Locate every Plasmodium malariae-infected red blood cell.
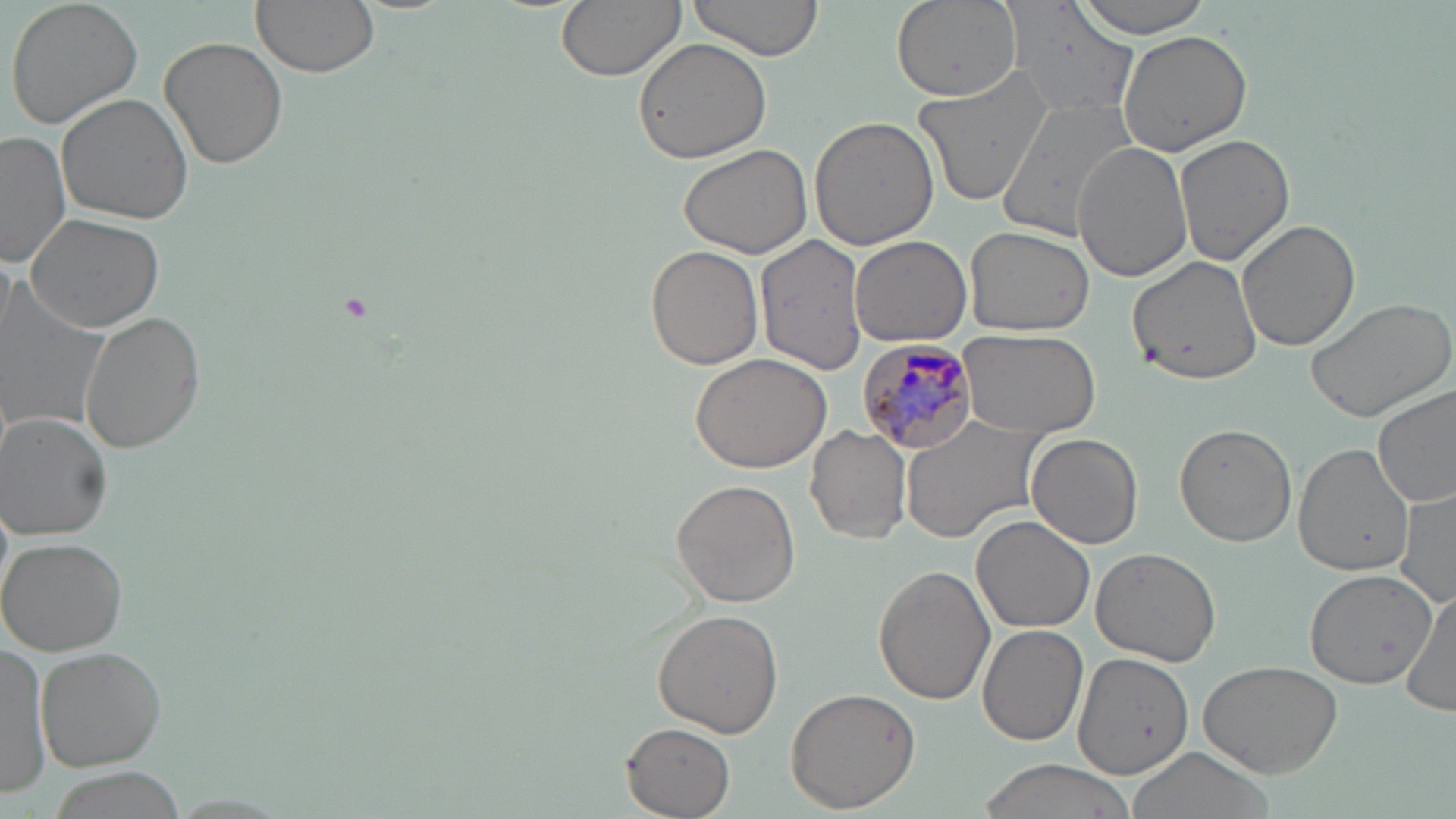
Approximate bounding boxes as (x1,y1)-(x2,y2) corner pairs in pixels.
Plasmodium malariae-infected red blood cells: (856,339)-(983,457).

slide-level diagnosis = Plasmodium malariae
preparation = thin blood smear
magnification = 1000x
stain = May-Grünwald-Giemsa
uninfected red blood cell locations = approximate bounding boxes as (x1,y1)-(x2,y2) corner pairs in pixels: (4,0)-(145,131), (251,0)-(378,77), (556,0)-(683,80), (684,0)-(827,65), (890,0)-(1022,102), (1069,0)-(1215,38), (1003,2)-(1138,117), (1118,29)-(1253,156), (159,36)-(290,170), (633,37)-(773,166), (914,69)-(1056,210), (57,93)-(193,225), (995,96)-(1140,242), (811,116)-(938,251), (0,131)-(72,268), (1174,134)-(1293,265), (676,141)-(812,258), (1073,142)-(1196,282), (27,212)-(167,332), (1236,219)-(1360,353), (964,223)-(1096,335), (755,236)-(870,376), (849,236)-(971,348), (644,246)-(762,370), (1126,252)-(1262,385), (1,276)-(111,434), (1304,295)-(1455,423), (78,310)-(206,454), (958,327)-(1099,438), (688,352)-(833,474), (1374,384)-(1456,509), (901,412)-(1047,543), (3,413)-(115,540), (1175,422)-(1297,546), (807,426)-(912,545), (1027,433)-(1144,549), (1293,441)-(1416,576), (671,479)-(802,608), (1398,488)-(1456,610), (972,515)-(1094,635), (2,537)-(127,656), (1092,544)-(1225,665), (874,566)-(995,704), (1303,570)-(1438,689), (1405,590)-(1455,717), (652,609)-(784,735), (977,625)-(1087,748), (0,641)-(52,795), (33,645)-(167,771), (1071,652)-(1238,780), (1196,659)-(1344,776), (785,686)-(920,813), (621,723)-(736,816), (1123,746)-(1277,819), (972,759)-(1146,819)
field of view = single
image size = 1456×819 pixels
modality = optical microscopy